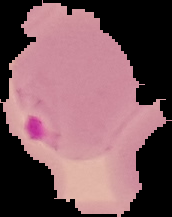

Summary:
  - Result: malaria parasites detected
  - Image type: segmented cell region with the area outside set to black
  - Image size: 172×217 pixels
  - Preparation: thin blood film